Report the malaria status of this cell.
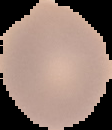
Uninfected.

From a thin blood smear. Image is 112×130 pixels. The area outside the segmented cell region is set to black.